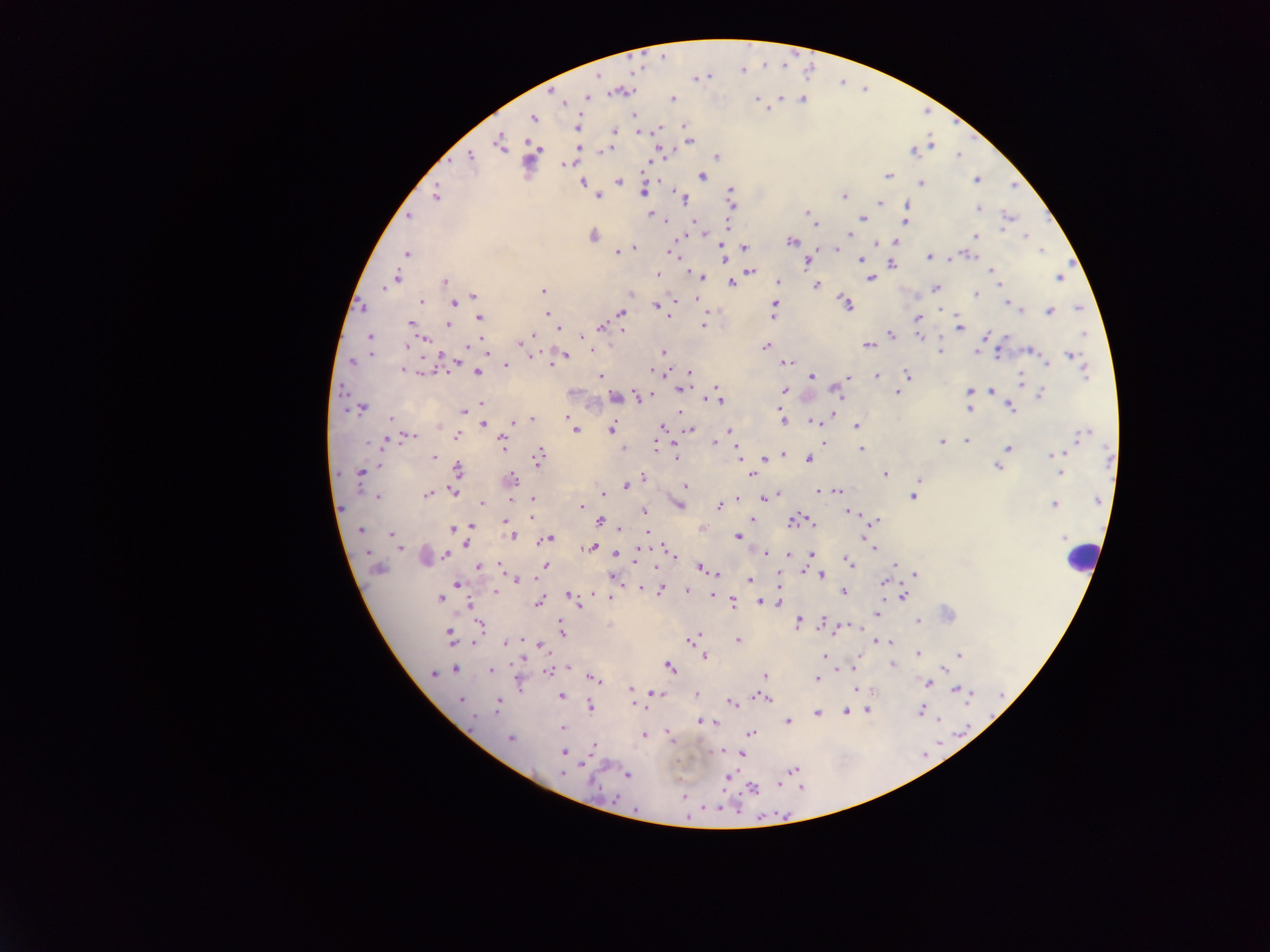

Approximate centers as [x, y] in pixels.
Summary:
  - Malaria parasite locations: [741, 69], [697, 77], [620, 91], [587, 97], [781, 97], [673, 98], [757, 99], [803, 99], [563, 103], [635, 115], [532, 118], [684, 126], [577, 127], [660, 128], [614, 131], [639, 132], [689, 141], [500, 143], [932, 145], [607, 149], [914, 152], [959, 155], [470, 157], [716, 157], [565, 165], [888, 175], [702, 177], [976, 179], [582, 182], [618, 182], [922, 183], [644, 191], [730, 191], [435, 196], [599, 196], [843, 196], [683, 198], [880, 203], [731, 204], [906, 208], [978, 208], [807, 211], [651, 214], [408, 216], [1007, 217], [862, 218], [905, 221], [813, 222], [726, 225], [850, 235], [593, 236], [975, 236], [1025, 236], [792, 241], [895, 241], [839, 245], [745, 247], [634, 248], [836, 249], [627, 250], [1042, 251], [617, 252], [671, 253], [407, 254], [969, 255], [724, 256], [929, 257], [860, 260], [809, 262], [893, 265], [751, 271], [991, 271], [658, 274], [700, 276], [1059, 277], [397, 278], [871, 278], [995, 279], [778, 281], [445, 282], [731, 283], [387, 285], [816, 285], [936, 288], [384, 289], [542, 291], [630, 294], [975, 294], [473, 295], [696, 299], [421, 302], [846, 303], [1006, 303], [454, 304], [774, 305], [656, 306], [1079, 307], [1019, 309], [1050, 311], [620, 312], [774, 314], [546, 315], [480, 318], [917, 318], [410, 323], [448, 324], [703, 325], [601, 327], [559, 328], [959, 328], [622, 330], [990, 334], [891, 335], [919, 335], [1085, 335], [582, 336], [370, 337], [533, 337], [425, 339], [520, 342], [407, 346], [470, 346], [867, 346], [765, 347], [940, 351], [977, 351], [1029, 351], [664, 352], [370, 353], [1071, 355], [531, 356], [565, 356], [352, 362], [787, 363], [1047, 363], [551, 364], [506, 366], [403, 370], [477, 372], [653, 372], [1084, 372], [689, 373], [907, 374], [600, 376], [812, 377], [849, 377], [876, 377], [1021, 379], [681, 389], [785, 391], [835, 391], [970, 391], [991, 391], [898, 393], [1040, 395], [615, 397], [639, 398], [717, 399], [481, 403], [1010, 407], [363, 409], [970, 410], [464, 411], [391, 418], [567, 418], [782, 418], [531, 419], [520, 420], [813, 421], [483, 425], [856, 427], [662, 428], [575, 429], [611, 430], [690, 430], [730, 431], [457, 435], [1083, 435], [412, 436], [502, 440], [823, 440], [386, 441], [713, 442], [941, 442], [966, 442], [656, 447], [623, 448], [1008, 448], [861, 449], [783, 454], [1057, 454], [434, 457], [539, 457], [676, 457], [1108, 457], [765, 459], [808, 460], [378, 465], [997, 467], [458, 470], [360, 473], [1060, 473], [750, 474], [885, 475], [642, 476], [511, 480], [918, 480], [684, 485], [626, 486], [821, 491], [836, 491], [453, 492], [427, 495], [604, 495], [777, 495], [378, 497], [913, 497], [764, 498], [533, 499], [511, 500], [680, 500], [1098, 501], [482, 504], [1054, 505], [581, 506], [679, 506], [720, 506], [644, 510], [849, 513], [532, 517], [601, 520], [751, 520], [795, 521], [876, 521], [504, 522], [473, 527], [453, 528], [620, 529], [360, 530], [647, 532], [391, 534], [512, 536], [738, 537], [548, 539], [865, 539], [466, 543], [400, 548], [588, 548], [874, 548], [368, 553], [616, 553], [668, 553], [672, 554], [766, 554], [811, 554], [446, 555], [789, 555], [635, 559], [848, 561], [545, 565], [895, 565], [479, 567], [703, 570], [804, 572], [916, 574], [821, 576], [750, 579], [517, 580], [884, 582], [456, 585], [640, 588], [661, 590], [687, 591], [496, 592], [844, 592], [592, 593], [569, 596], [713, 596], [903, 596], [609, 597], [439, 599], [733, 602], [761, 602], [538, 603], [470, 605], [577, 605], [877, 615], [918, 621], [798, 623], [823, 623], [480, 626], [562, 632], [449, 634], [693, 639], [738, 640], [889, 642], [506, 643], [539, 647], [918, 653], [959, 655], [705, 656], [825, 657], [892, 666], [669, 667], [852, 668], [944, 668], [455, 669], [490, 670], [549, 671], [432, 674], [764, 676], [595, 678], [816, 680], [927, 684], [630, 689], [857, 690], [960, 691], [655, 692], [696, 695], [561, 697], [764, 699], [461, 700], [499, 703], [634, 704], [731, 704], [590, 707], [868, 711], [845, 712], [920, 712], [817, 714], [700, 721], [788, 721], [563, 728], [751, 734], [644, 735], [511, 738], [670, 738], [594, 745], [564, 753], [742, 754], [794, 770], [562, 773], [627, 775], [727, 778], [753, 788], [721, 808]
  - Leukocyte locations: [426, 554], [1082, 556]
  - Country: Ghana
  - Capture: mobile-phone photograph through a microscope
  - Image size: 1270×952 pixels
  - Preparation: thick blood smear
  - Field of view: single